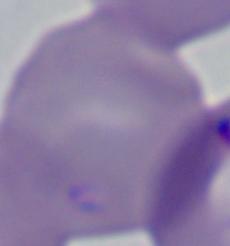

1000x magnification. A Babesia parasite is shown. Photomicrograph.